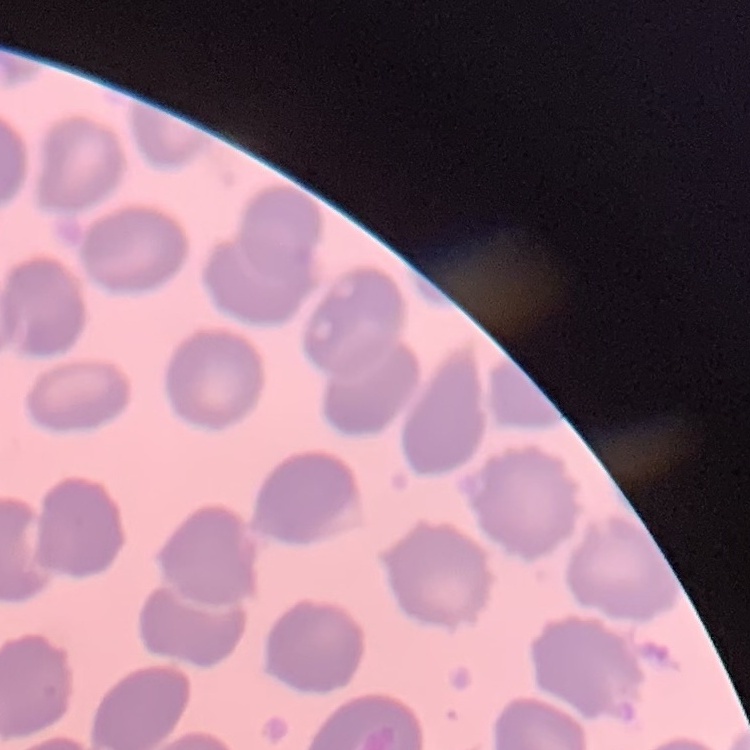
{
  "red_blood_cell_morphology": "no rouleaux formation",
  "image_type": "one tile cut from a larger photomicrograph",
  "preparation": "thin blood film",
  "stain": "Field's or Giemsa"
}